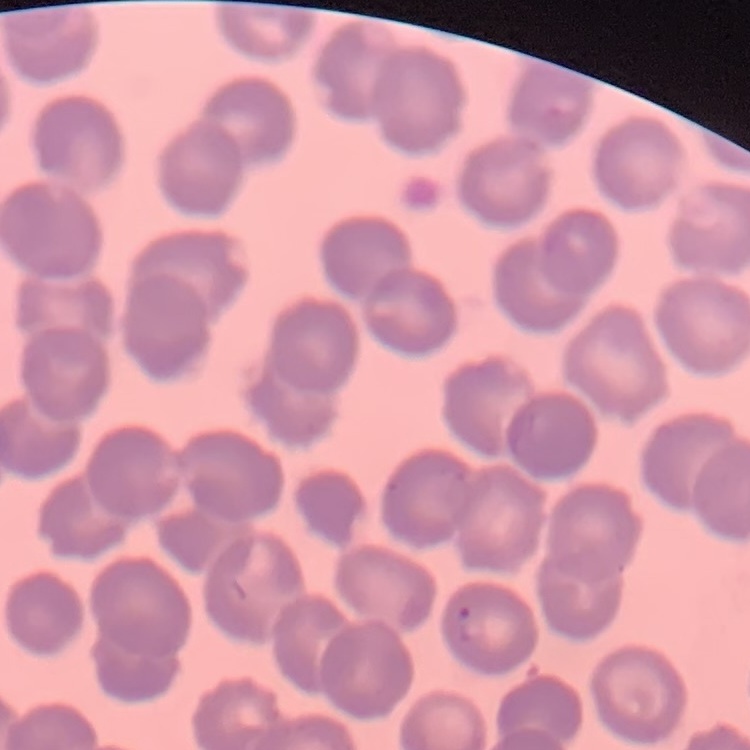

Summary:
  - Red blood cell morphology: no rouleaux formation
  - Image type: square crop of a larger photomicrograph
  - Stain: Field's or Giemsa
  - Preparation: thin blood smear